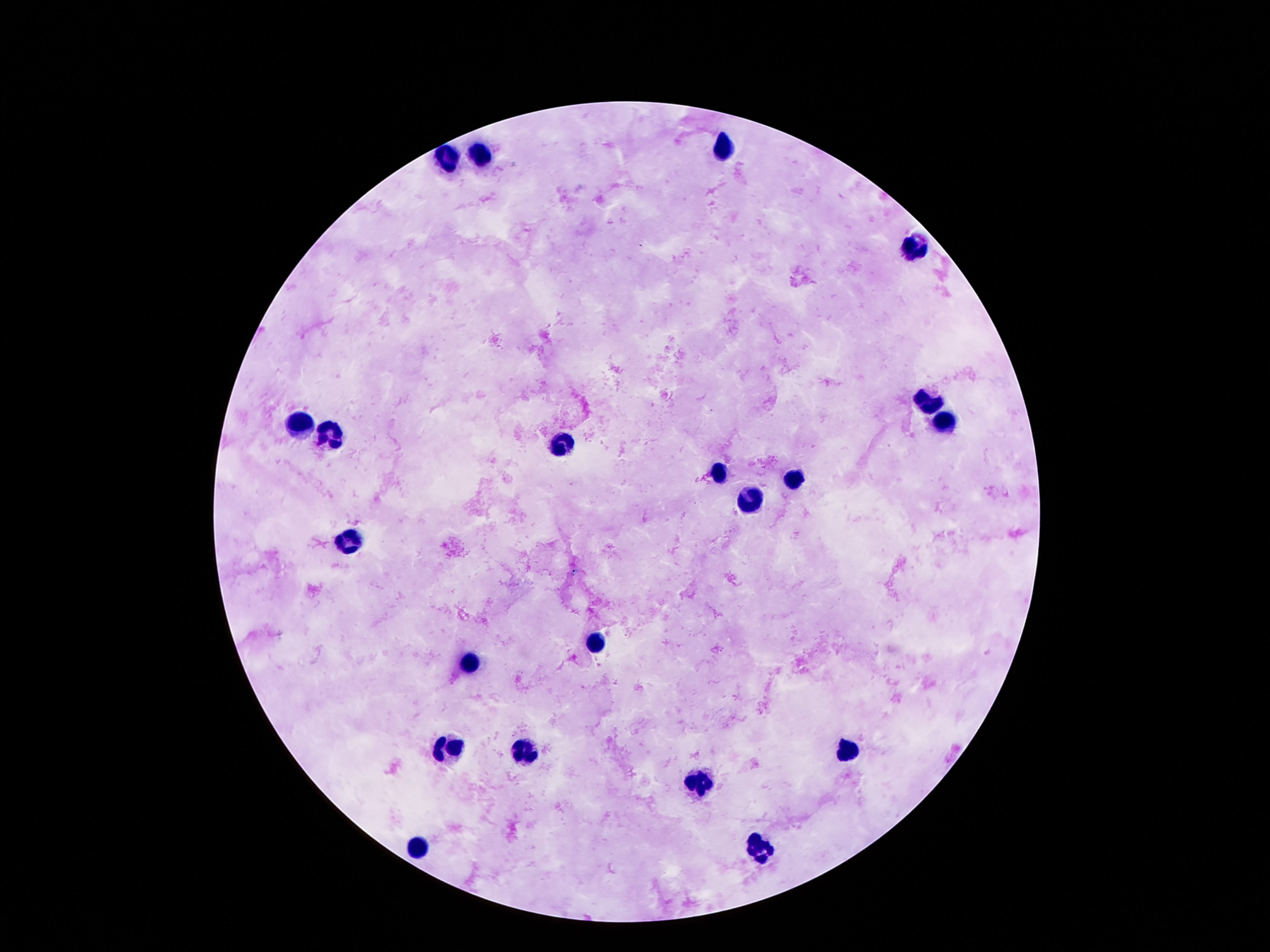
Approximate centers as (x, y) in pixels. Leukocyte locations: (721, 147), (481, 153), (445, 156), (912, 246), (927, 401), (297, 423), (942, 423), (330, 436), (562, 447), (721, 474), (796, 479), (752, 501), (352, 540), (595, 643), (467, 664), (449, 749), (845, 753), (525, 754), (697, 786), (419, 848), (759, 849). Image is 1270×952 pixels. 100x magnification. Thick blood film. Giemsa-stained preparation. Single field of view. Patient malaria status: not infected. Photographed through the microscope eyepiece with a smartphone camera.